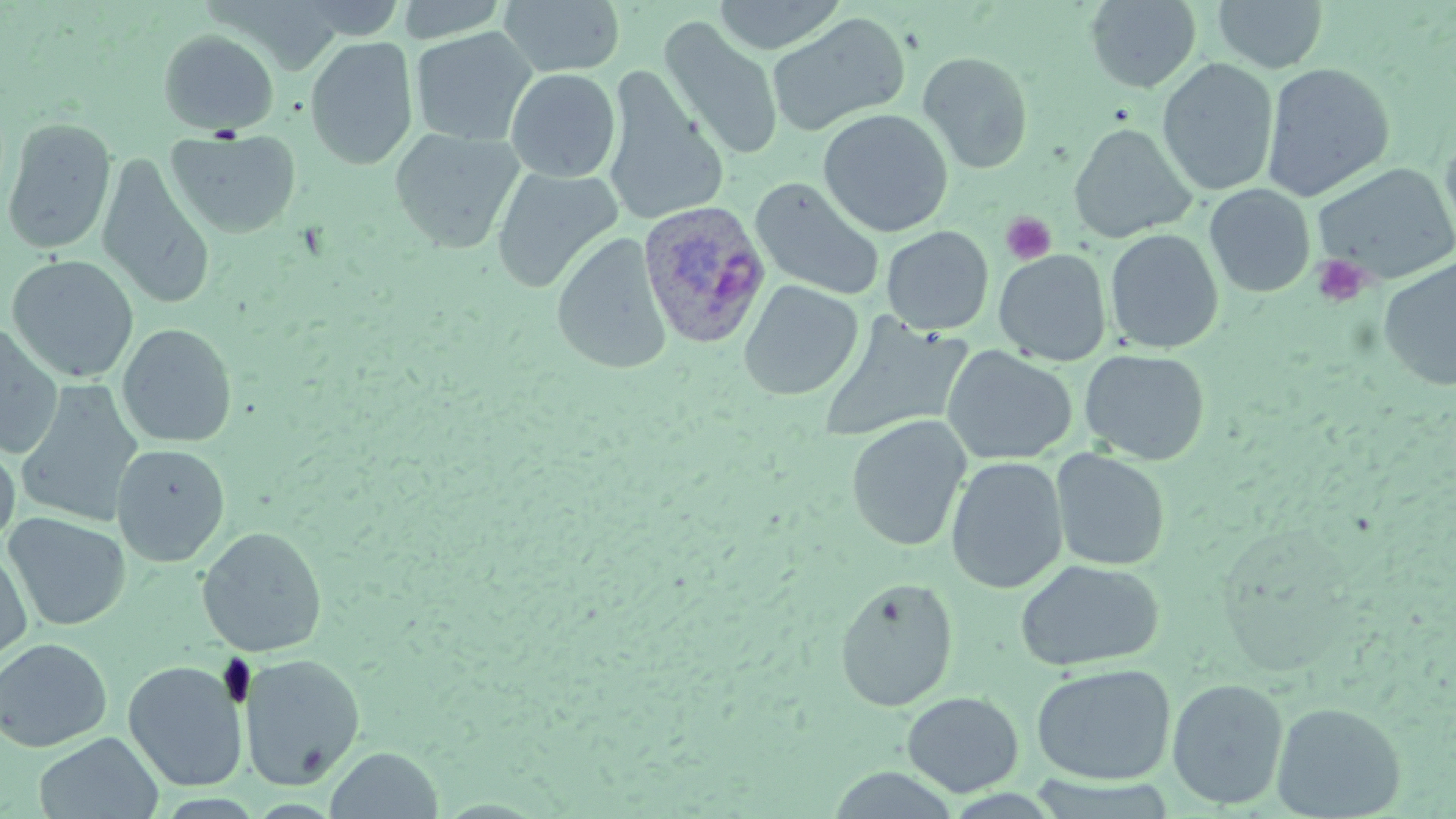

slide-level diagnosis = Plasmodium ovale
preparation = thin blood smear
image size = 1456×819 pixels
magnification = 1000x
uninfected red blood cell locations = approximate bounding boxes as named x1/y1/x2/y2 corners in pixels: (x1=498, y1=0, x2=626, y2=76), (x1=712, y1=0, x2=847, y2=55), (x1=1211, y1=0, x2=1329, y2=73), (x1=1085, y1=1, x2=1202, y2=92), (x1=766, y1=11, x2=911, y2=136), (x1=660, y1=18, x2=783, y2=161), (x1=410, y1=27, x2=537, y2=146), (x1=158, y1=29, x2=279, y2=135), (x1=304, y1=35, x2=418, y2=171), (x1=918, y1=51, x2=1034, y2=174), (x1=1157, y1=57, x2=1279, y2=196), (x1=1262, y1=62, x2=1395, y2=202), (x1=505, y1=68, x2=621, y2=183), (x1=603, y1=75, x2=729, y2=228), (x1=818, y1=109, x2=953, y2=237), (x1=1, y1=117, x2=117, y2=255), (x1=1069, y1=123, x2=1196, y2=242), (x1=390, y1=127, x2=524, y2=252), (x1=167, y1=128, x2=301, y2=239), (x1=1439, y1=130, x2=1456, y2=260), (x1=97, y1=152, x2=216, y2=311), (x1=1311, y1=162, x2=1456, y2=284), (x1=490, y1=167, x2=623, y2=293), (x1=750, y1=177, x2=885, y2=301), (x1=1204, y1=184, x2=1315, y2=298), (x1=881, y1=226, x2=994, y2=335), (x1=1104, y1=228, x2=1223, y2=353), (x1=552, y1=232, x2=672, y2=374), (x1=994, y1=249, x2=1111, y2=365), (x1=6, y1=255, x2=139, y2=383), (x1=1377, y1=256, x2=1456, y2=392), (x1=738, y1=280, x2=863, y2=400), (x1=817, y1=314, x2=972, y2=444), (x1=0, y1=323, x2=64, y2=459), (x1=117, y1=323, x2=237, y2=447), (x1=941, y1=345, x2=1077, y2=465), (x1=1080, y1=349, x2=1211, y2=465), (x1=15, y1=380, x2=144, y2=527), (x1=846, y1=416, x2=970, y2=552), (x1=0, y1=437, x2=20, y2=547), (x1=111, y1=444, x2=230, y2=567), (x1=1051, y1=449, x2=1171, y2=571), (x1=945, y1=455, x2=1068, y2=594), (x1=3, y1=513, x2=131, y2=631), (x1=197, y1=526, x2=327, y2=657), (x1=0, y1=546, x2=33, y2=663), (x1=1015, y1=559, x2=1164, y2=672), (x1=834, y1=577, x2=958, y2=712), (x1=0, y1=637, x2=112, y2=752), (x1=239, y1=654, x2=365, y2=789), (x1=123, y1=661, x2=248, y2=791), (x1=1031, y1=663, x2=1176, y2=785), (x1=1166, y1=678, x2=1288, y2=809), (x1=901, y1=691, x2=1023, y2=797), (x1=1271, y1=701, x2=1406, y2=818), (x1=34, y1=732, x2=164, y2=818), (x1=325, y1=746, x2=444, y2=819), (x1=824, y1=767, x2=962, y2=818)
platelet locations = approximate bounding boxes as named x1/y1/x2/y2 corners in pixels: (x1=1000, y1=211, x2=1057, y2=265), (x1=1311, y1=254, x2=1371, y2=308)
stain = May-Grünwald-Giemsa
Plasmodium ovale-infected red blood cell locations = approximate bounding boxes as named x1/y1/x2/y2 corners in pixels: (x1=637, y1=200, x2=771, y2=349)
field of view = one of a larger specimen
modality = optical microscopy